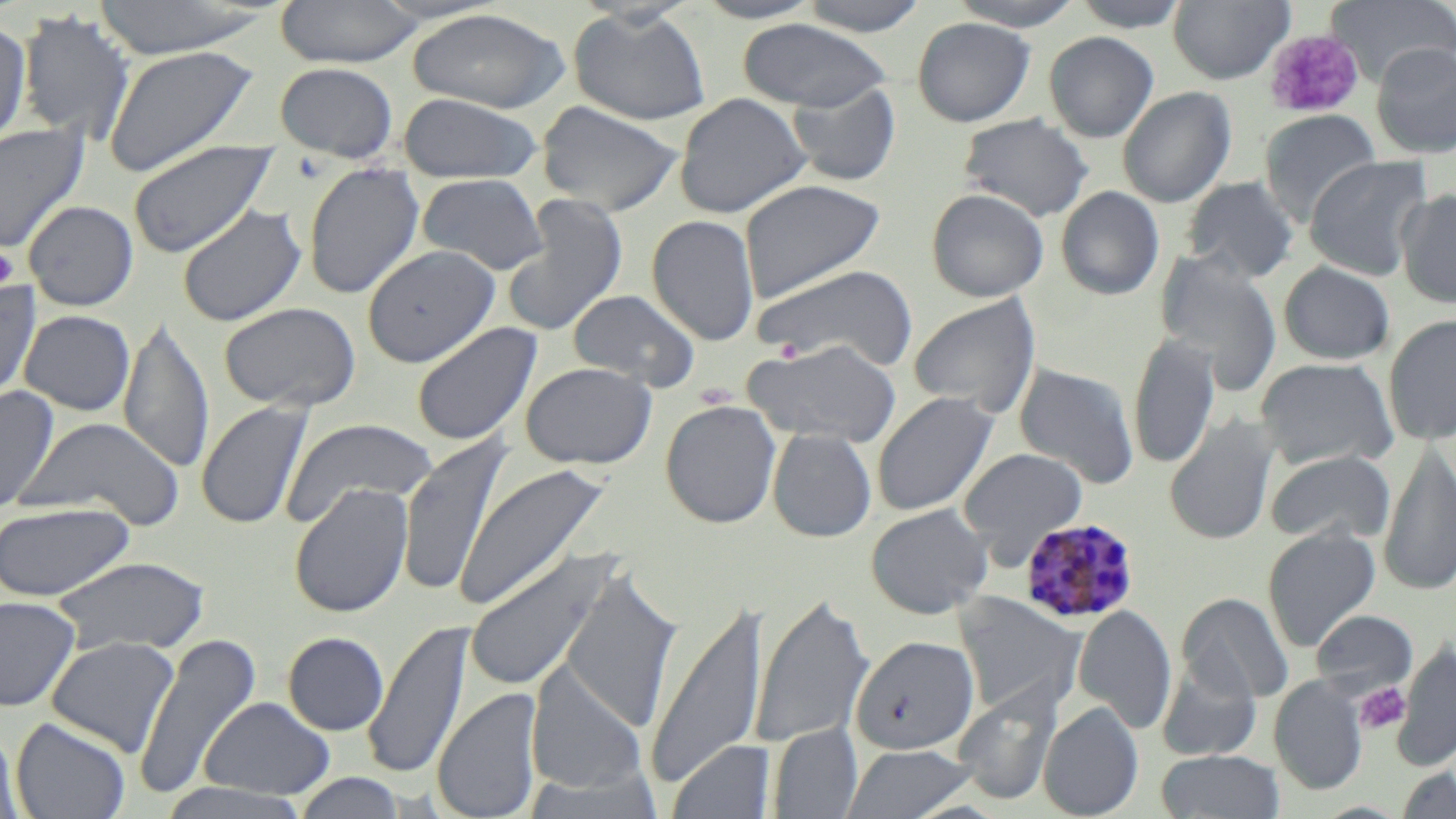
Summary:
  - Coordinate format: approximate bounding boxes as [x1, y1, x2, y2] in pixels
  - Uninfected red blood cell locations: [88, 0, 275, 58], [275, 0, 425, 68], [693, 0, 826, 23], [796, 0, 931, 35], [947, 0, 1087, 30], [1070, 0, 1190, 32], [1168, 0, 1294, 84], [1325, 0, 1456, 86], [568, 7, 711, 126], [406, 8, 570, 113], [16, 10, 136, 145], [912, 16, 1036, 127], [0, 18, 33, 151], [737, 18, 894, 112], [1044, 32, 1159, 143], [1371, 42, 1456, 158], [103, 44, 260, 178], [274, 62, 399, 163], [786, 81, 901, 186], [1117, 87, 1236, 207], [398, 92, 542, 184], [673, 93, 812, 218], [535, 101, 685, 216], [1259, 109, 1381, 224], [958, 113, 1094, 221], [0, 123, 90, 255], [128, 139, 279, 259], [1304, 155, 1433, 281], [303, 162, 425, 300], [417, 173, 548, 275], [1182, 177, 1300, 283], [738, 179, 885, 302], [1055, 186, 1165, 300], [926, 188, 1049, 302], [1395, 189, 1456, 308], [502, 194, 629, 337], [23, 200, 139, 311], [177, 203, 306, 327], [646, 214, 760, 346], [362, 245, 500, 367], [1155, 250, 1283, 394], [1278, 261, 1395, 364], [752, 263, 920, 372], [0, 281, 41, 406], [567, 288, 701, 391], [908, 293, 1041, 418], [218, 302, 360, 412], [19, 310, 135, 416], [1383, 314, 1456, 445], [119, 317, 214, 475], [411, 322, 542, 447], [1129, 332, 1220, 469], [741, 339, 903, 447], [1255, 358, 1399, 471], [520, 362, 657, 470], [1013, 363, 1140, 487], [0, 385, 59, 514], [871, 392, 998, 516], [660, 399, 781, 529], [196, 401, 313, 530], [1164, 415, 1279, 546], [17, 417, 187, 529], [281, 418, 438, 528], [768, 428, 877, 543], [398, 435, 512, 598], [1377, 441, 1456, 596], [959, 448, 1087, 563], [1265, 450, 1395, 544], [455, 462, 610, 612], [289, 483, 414, 618], [0, 502, 134, 602], [866, 504, 992, 619], [1262, 526, 1381, 652], [463, 549, 616, 694], [50, 556, 211, 656], [559, 566, 684, 734], [750, 592, 874, 750], [955, 592, 1085, 718], [1176, 593, 1293, 704], [0, 595, 81, 712], [645, 600, 770, 789], [1073, 604, 1177, 734], [1310, 609, 1418, 698], [363, 621, 471, 781], [131, 631, 262, 801], [282, 632, 389, 736], [850, 635, 979, 755], [46, 636, 180, 757], [1390, 643, 1456, 772], [1156, 659, 1262, 762], [526, 665, 650, 796], [1268, 675, 1368, 795], [952, 684, 1061, 805], [432, 687, 543, 819], [199, 696, 335, 801], [1038, 703, 1143, 819], [10, 717, 131, 819], [1, 724, 26, 819], [768, 724, 862, 818], [668, 739, 775, 819], [841, 743, 977, 819], [1156, 749, 1284, 818], [1394, 766, 1456, 818], [293, 772, 406, 818], [150, 780, 318, 819]
  - Plasmodium malariae-infected red blood cell locations: [1020, 517, 1140, 624]
  - Platelet locations: [1264, 29, 1364, 119], [0, 246, 19, 290], [1356, 682, 1410, 734]
  - Slide-level diagnosis: Plasmodium malariae
  - Preparation: thin blood smear
  - Image size: 1456×819 pixels
  - Stain: May-Grünwald-Giemsa
  - Field of view: single
  - Modality: optical microscopy
  - Magnification: 1000x